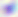

modality = micrograph
identification = Toxoplasma gondii
magnification = 400x